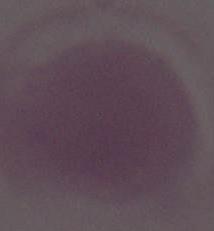

An erythrocyte is seen. Photomicrograph. 1000x magnification.